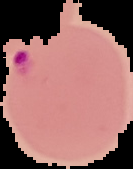
Summary:
  - Image type: segmented cell region on a black background
  - Malaria status: parasitized
  - Preparation: thin blood film
  - Image size: 133×169 pixels